Locate every leukocyte (white blood cell).
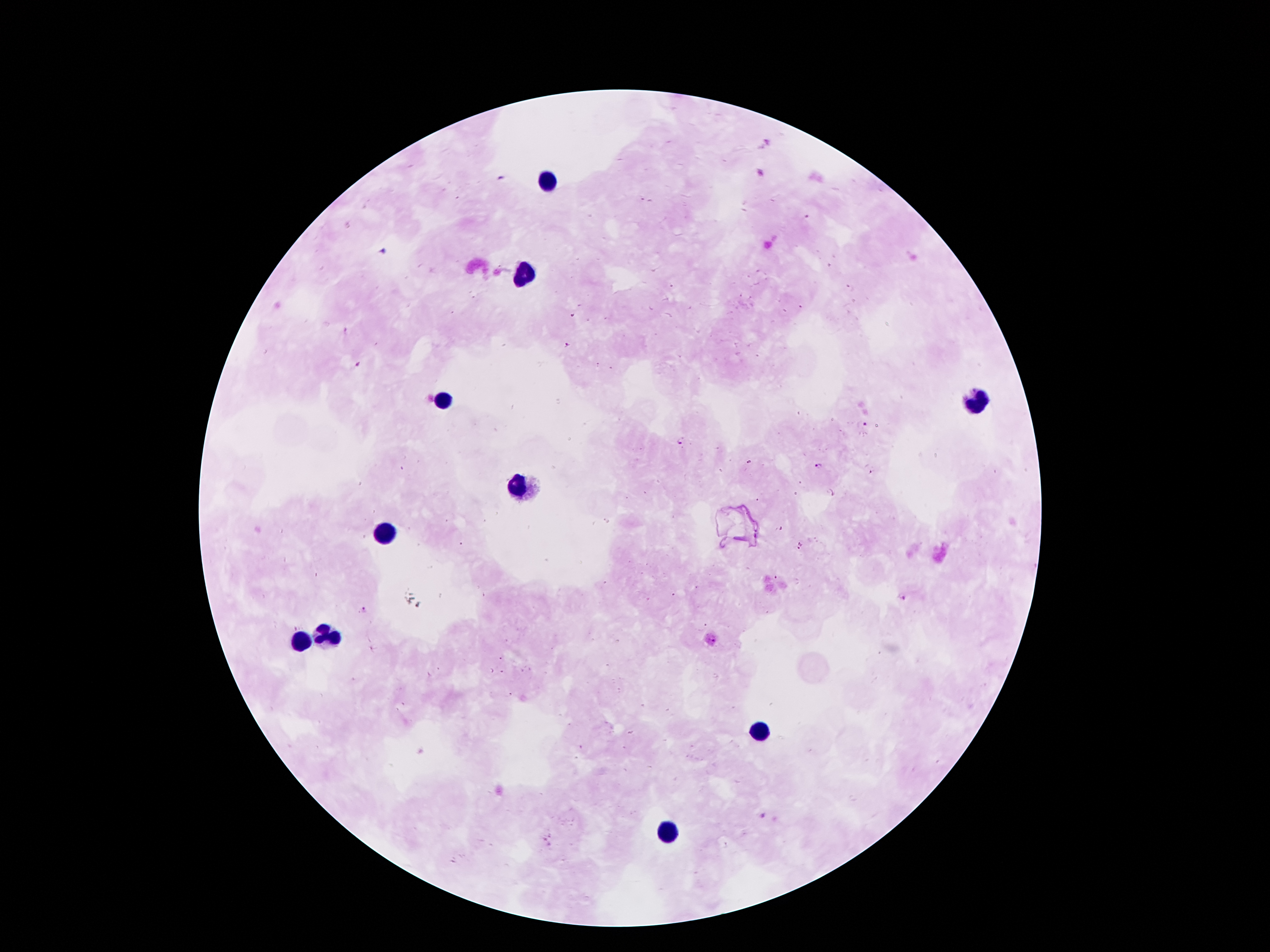

Approximate object centers, in pixels from the top-left corner.
Leukocytes: (x=549, y=178), (x=527, y=274), (x=978, y=401), (x=443, y=404), (x=520, y=485), (x=388, y=536), (x=330, y=634), (x=304, y=641), (x=760, y=728), (x=666, y=833).

Plasmodium parasite locations = (x=642, y=200), (x=807, y=217), (x=850, y=289), (x=800, y=307), (x=572, y=316), (x=569, y=346), (x=358, y=365), (x=865, y=425), (x=681, y=441), (x=819, y=466), (x=870, y=472), (x=780, y=528), (x=801, y=546), (x=776, y=577), (x=902, y=597), (x=364, y=609), (x=501, y=658), (x=762, y=817), (x=544, y=839)
patient malaria status = infected with Plasmodium falciparum
stain = Giemsa
magnification = 100x
field of view = single
image size = 1270×952 pixels
capture = smartphone camera through the microscope eyepiece
preparation = thick blood film